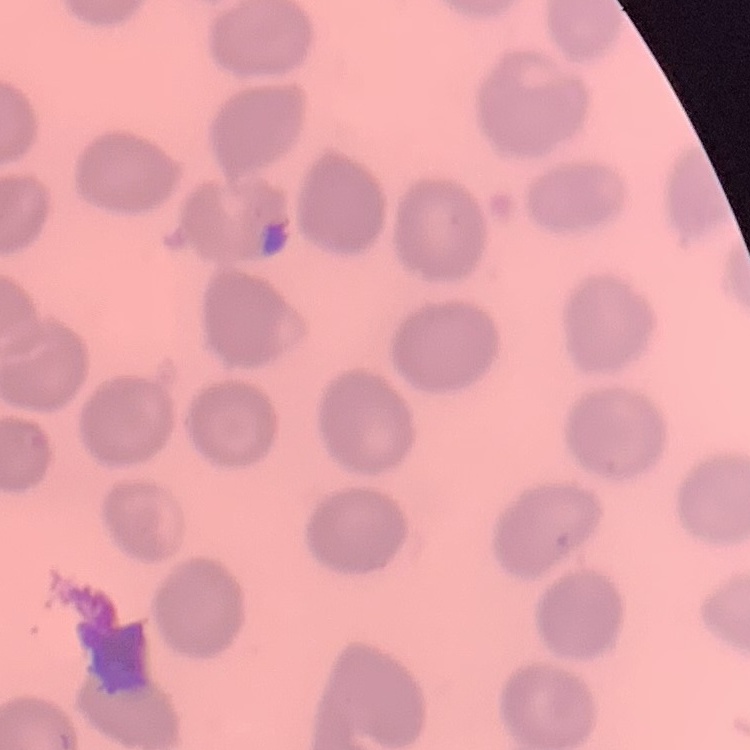

Summary:
  - Red blood cell morphology: no rouleaux formation
  - Image type: square crop of a larger photomicrograph
  - Stain: Field's or Giemsa
  - Preparation: thin peripheral smear